Classify this cell by malaria status.
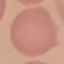
Uninfected.

Photographed with a smartphone camera at the microscope eyepiece. Giemsa-stained preparation. Cell patch, automatically extracted from a larger field of view and resized to 64 × 64 pixels. Thin blood smear.